Report the malaria status of this cell.
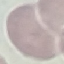

It is uninfected.

image type = automatically extracted cell patch, resized to 64 × 64 pixels
stain = Giemsa
capture = smartphone through the microscope eyepiece
preparation = thin blood smear